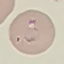

Result: malaria parasites identified. Giemsa-stained preparation. Cell patch, automatically extracted from a larger field of view and resized to 64 × 64 pixels. Thin blood smear. Acquired by smartphone through the microscope eyepiece.